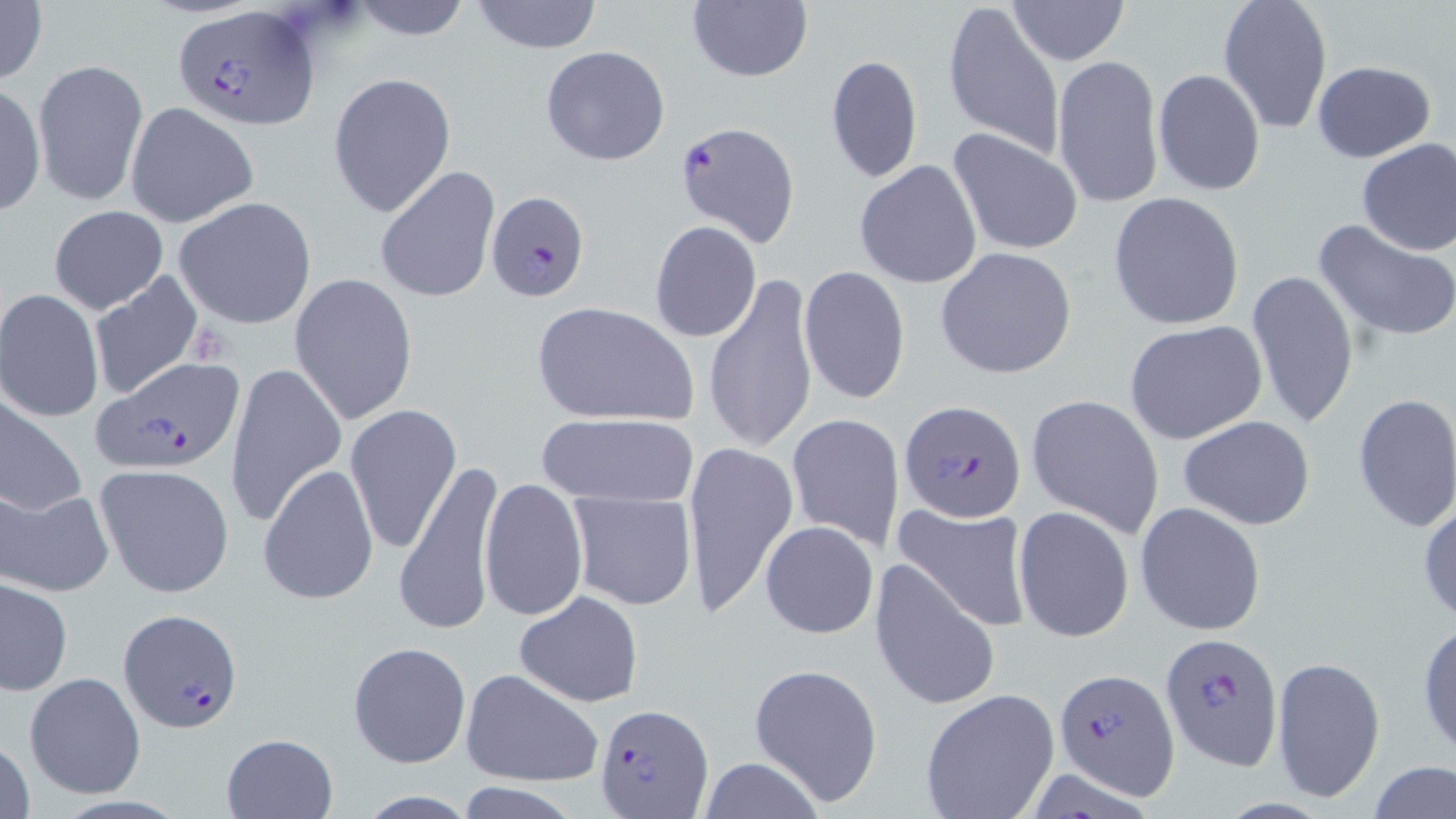

Summary:
  - Coordinate format: approximate bounding boxes as (x1,y1)-(x2,y2) corner pairs in pixels
  - Platelet locations: (188,325)-(234,365)
  - Plasmodium falciparum-infected red blood cell locations: (172,5)-(317,130), (673,121)-(802,249), (485,191)-(592,304), (95,359)-(245,475), (900,398)-(1029,523), (117,609)-(244,734), (1159,634)-(1282,768), (1053,668)-(1180,795), (594,703)-(713,817)
  - Uninfected red blood cell locations: (0,0)-(47,84), (348,0)-(474,41), (468,0)-(606,53), (1216,0)-(1334,134), (941,1)-(1066,163), (1006,1)-(1130,65), (685,2)-(815,84), (539,46)-(672,165), (823,54)-(921,187), (1051,54)-(1165,209), (32,58)-(148,207), (1312,60)-(1435,162), (1152,70)-(1265,194), (327,71)-(457,218), (834,73)-(948,249), (0,83)-(46,217), (124,101)-(258,229), (947,127)-(1085,257), (1355,137)-(1456,255), (854,160)-(983,287), (374,166)-(500,305), (1107,191)-(1246,331), (174,196)-(317,330), (49,205)-(169,315), (1313,217)-(1456,346), (649,221)-(763,343), (936,247)-(1077,380), (798,266)-(910,404), (88,268)-(203,401), (1245,269)-(1360,430), (289,273)-(419,425), (703,273)-(819,456), (0,289)-(104,422), (531,300)-(699,426), (1124,320)-(1269,446), (226,361)-(347,525), (1025,392)-(1166,539), (0,393)-(87,521), (1352,393)-(1456,533), (343,403)-(462,554), (534,411)-(699,508), (785,411)-(905,553), (1177,416)-(1315,531), (683,443)-(798,620), (393,459)-(506,637), (94,463)-(235,599), (258,463)-(380,604), (480,476)-(588,621), (0,487)-(115,598), (567,491)-(697,610), (1418,494)-(1456,629), (892,500)-(1032,631), (1135,502)-(1266,636), (1014,507)-(1135,642), (759,520)-(879,639), (869,557)-(1000,713), (1,578)-(73,696), (514,592)-(642,706), (1416,619)-(1456,760), (348,640)-(471,768), (344,655)-(591,776), (1271,656)-(1385,805), (748,663)-(882,807), (461,669)-(605,786), (23,671)-(146,799), (919,688)-(1059,819), (221,733)-(337,817), (0,736)-(36,819), (695,758)-(828,818), (1368,760)-(1455,817), (457,782)-(578,818), (354,790)-(480,817)
  - Slide-level diagnosis: Plasmodium falciparum
  - Modality: optical microscopy
  - Magnification: 1000x
  - Preparation: thin blood film
  - Stain: May-Grünwald-Giemsa
  - Field of view: single
  - Image size: 1456×819 pixels